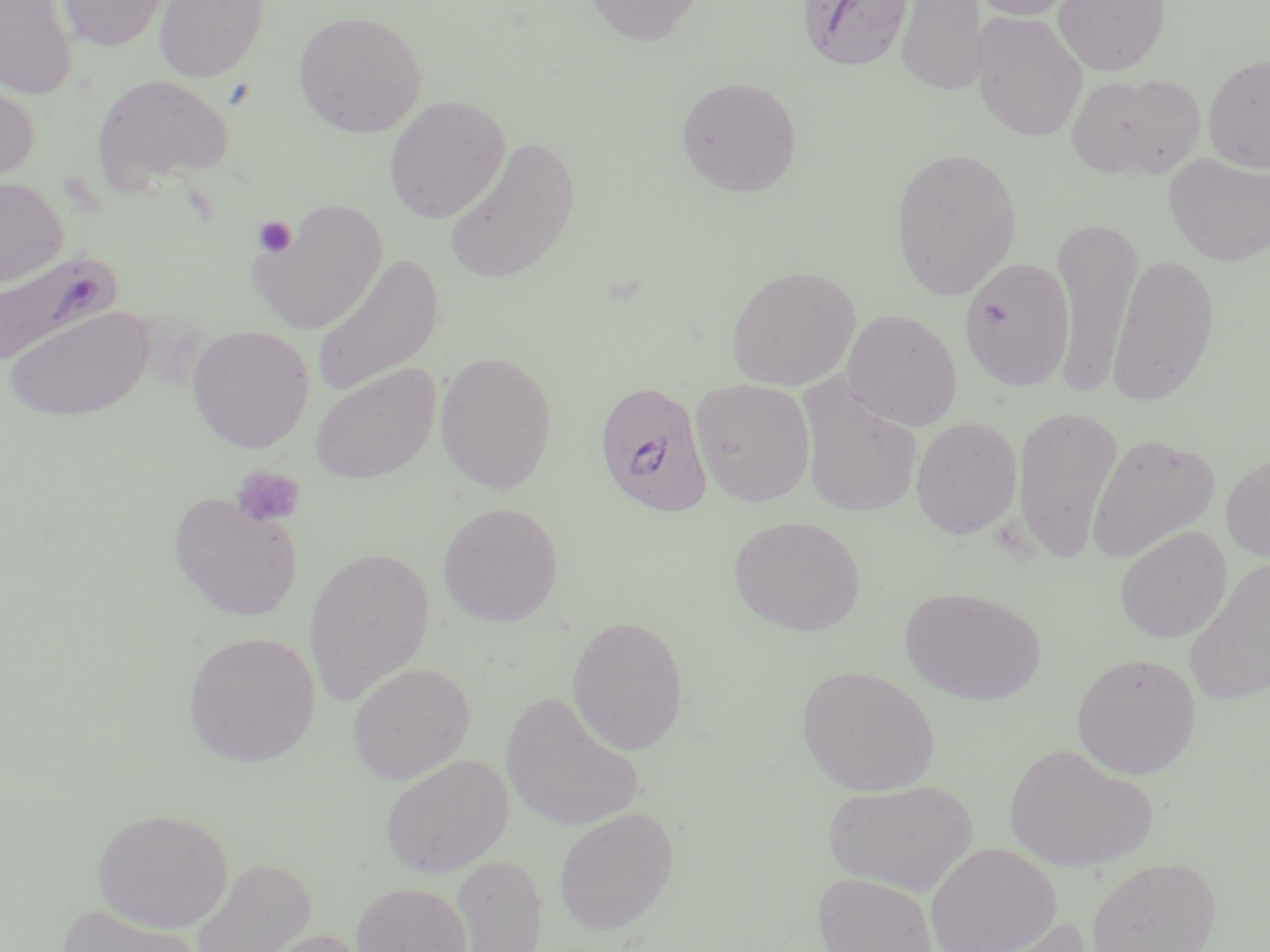

Summary:
  - Coordinate format: approximate bounding boxes as [x1, y1, x2, y2] in pixels
  - Uninfected red blood cell locations: [56, 0, 175, 52], [154, 0, 268, 82], [583, 0, 708, 45], [895, 0, 985, 97], [967, 0, 1082, 21], [1052, 0, 1171, 76], [1, 1, 78, 100], [293, 10, 427, 138], [972, 11, 1088, 142], [1203, 52, 1270, 174], [1066, 71, 1206, 181], [89, 74, 234, 193], [0, 75, 40, 188], [676, 76, 802, 198], [384, 95, 511, 223], [443, 136, 581, 284], [890, 146, 1023, 301], [1164, 153, 1270, 267], [0, 177, 68, 288], [248, 198, 387, 335], [1050, 215, 1143, 394], [308, 252, 444, 401], [1107, 252, 1221, 406], [958, 257, 1075, 392], [726, 265, 861, 391], [4, 305, 154, 422], [842, 308, 963, 430], [186, 325, 315, 453], [433, 350, 558, 495], [309, 363, 441, 485], [796, 376, 923, 518], [690, 378, 815, 507], [1012, 405, 1122, 563], [911, 417, 1023, 540], [1086, 431, 1221, 565], [1220, 449, 1270, 563], [167, 492, 303, 622], [437, 502, 564, 627], [729, 515, 866, 637], [1114, 526, 1232, 643], [303, 545, 436, 708], [1184, 553, 1270, 706], [901, 586, 1046, 705], [567, 614, 689, 756], [183, 631, 321, 768], [1071, 652, 1202, 780], [347, 662, 475, 784], [796, 665, 940, 796], [501, 690, 646, 832], [1003, 742, 1159, 872], [380, 754, 513, 877], [822, 778, 980, 896], [91, 807, 233, 933], [553, 807, 680, 934], [925, 842, 1062, 952], [448, 854, 547, 951], [1087, 857, 1222, 952], [190, 859, 316, 952], [811, 871, 938, 952], [351, 882, 471, 952], [54, 904, 205, 952], [968, 916, 1094, 952], [256, 928, 373, 952]
  - Plasmodium falciparum-infected red blood cell locations: [798, 0, 915, 72], [0, 253, 120, 382], [594, 379, 713, 517]
  - Platelet locations: [252, 215, 299, 257], [232, 466, 305, 527]
  - Slide-level diagnosis: Plasmodium falciparum
  - Stain: May-Grünwald-Giemsa
  - Preparation: thin blood film
  - Modality: optical microscopy
  - Field of view: one of a larger specimen
  - Magnification: 1000x
  - Image size: 1270×952 pixels